State which parasite is depicted.
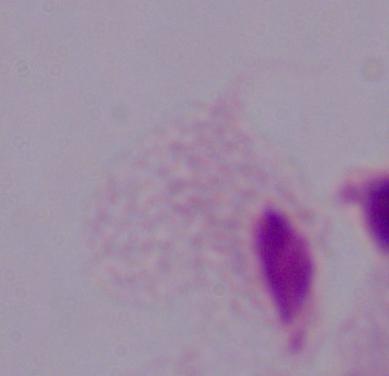
A trichomonad.

magnification = 1000x
modality = micrograph